Give the position of every malaria parasite and every leukocyte.
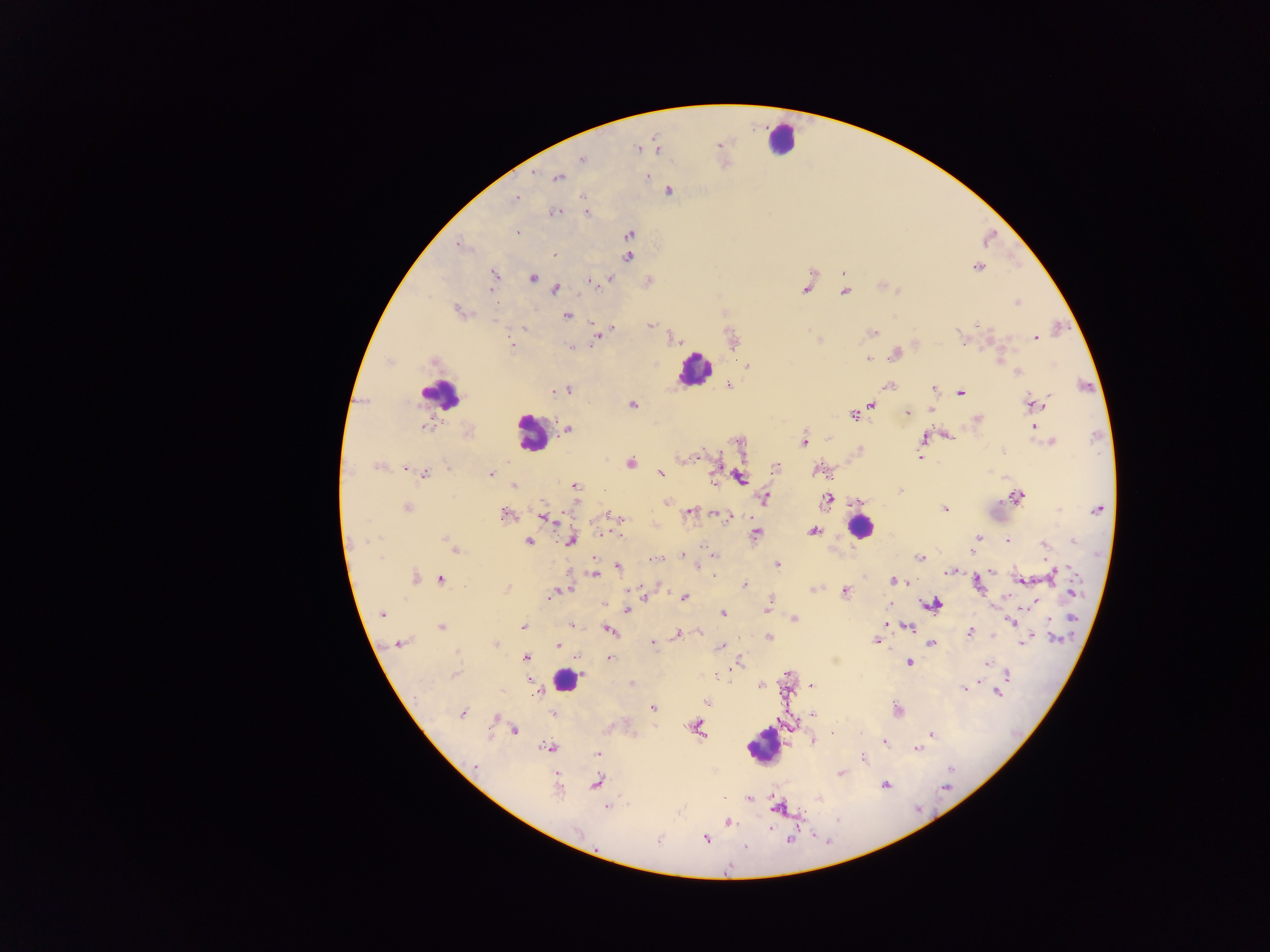

Approximate centers as {x, y} in pixels.
Malaria parasites: {719, 144}, {637, 148}, {657, 149}, {583, 160}, {647, 176}, {557, 177}, {668, 191}, {515, 198}, {554, 212}, {586, 212}, {516, 231}, {629, 234}, {458, 245}, {555, 256}, {629, 257}, {978, 268}, {494, 274}, {532, 278}, {609, 279}, {591, 281}, {806, 287}, {555, 289}, {490, 290}, {846, 291}, {1017, 302}, {456, 311}, {567, 315}, {593, 322}, {650, 325}, {977, 325}, {524, 328}, {613, 328}, {872, 333}, {960, 334}, {598, 337}, {674, 339}, {1036, 339}, {511, 343}, {570, 347}, {895, 354}, {867, 359}, {433, 362}, {747, 366}, {1018, 373}, {729, 385}, {888, 386}, {568, 389}, {933, 389}, {556, 391}, {960, 393}, {1032, 404}, {632, 405}, {872, 405}, {907, 412}, {853, 415}, {977, 419}, {1034, 425}, {425, 427}, {568, 429}, {947, 435}, {922, 438}, {1050, 441}, {803, 442}, {739, 443}, {1003, 451}, {697, 457}, {920, 458}, {631, 463}, {378, 466}, {447, 467}, {776, 468}, {406, 469}, {818, 470}, {660, 473}, {490, 474}, {424, 475}, {740, 478}, {714, 481}, {514, 486}, {575, 486}, {900, 491}, {1016, 497}, {765, 498}, {858, 500}, {827, 501}, {668, 503}, {407, 508}, {945, 508}, {1098, 509}, {1059, 510}, {690, 513}, {505, 515}, {718, 515}, {543, 516}, {607, 516}, {728, 517}, {813, 531}, {756, 533}, {605, 534}, {978, 538}, {1008, 540}, {363, 541}, {571, 541}, {1073, 541}, {529, 542}, {449, 544}, {1043, 544}, {455, 549}, {973, 550}, {682, 555}, {714, 556}, {921, 557}, {654, 559}, {777, 565}, {618, 567}, {992, 571}, {948, 572}, {595, 574}, {1054, 574}, {715, 576}, {416, 577}, {440, 579}, {1022, 580}, {893, 581}, {904, 581}, {908, 583}, {744, 584}, {978, 585}, {507, 588}, {814, 589}, {564, 591}, {845, 591}, {1072, 592}, {553, 594}, {645, 594}, {684, 597}, {933, 605}, {627, 609}, {766, 610}, {382, 614}, {723, 614}, {1072, 617}, {795, 619}, {1011, 621}, {886, 623}, {571, 625}, {523, 626}, {441, 627}, {909, 627}, {610, 631}, {970, 633}, {677, 634}, {769, 637}, {1056, 639}, {876, 640}, {1024, 641}, {401, 643}, {559, 643}, {495, 644}, {653, 644}, {932, 644}, {720, 647}, {457, 652}, {609, 657}, {526, 658}, {739, 662}, {909, 663}, {988, 663}, {453, 675}, {1008, 675}, {528, 681}, {631, 684}, {812, 686}, {965, 687}, {996, 693}, {535, 694}, {707, 702}, {652, 708}, {897, 711}, {463, 713}, {553, 714}, {813, 714}, {496, 718}, {696, 727}, {513, 730}, {832, 732}, {932, 734}, {813, 742}, {884, 742}, {550, 748}, {917, 748}, {598, 754}, {864, 759}, {475, 767}, {950, 769}, {841, 774}, {596, 783}, {885, 785}, {945, 787}, {558, 790}, {750, 798}, {819, 799}, {607, 807}, {780, 807}, {728, 823}, {577, 832}, {790, 839}, {706, 840}, {658, 841}, {746, 847}.
Leukocytes: {780, 139}, {695, 371}, {441, 394}, {531, 433}, {860, 527}, {567, 679}, {761, 745}.

{
  "field_of_view": "single",
  "preparation": "thick blood film",
  "image_size": "1270×952 pixels",
  "country": "Ghana",
  "capture": "mobile-phone photograph through a microscope"
}